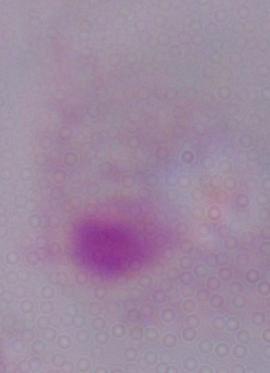
{
  "modality": "micrograph",
  "identification": "trichomonad",
  "magnification": "1000x"
}